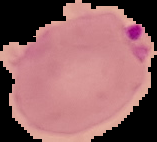
From a thin blood film. Image is 157×142 pixels. Segmented cell region on a black background. Malaria status: parasitized.